Describe the morphology of the red blood cells.
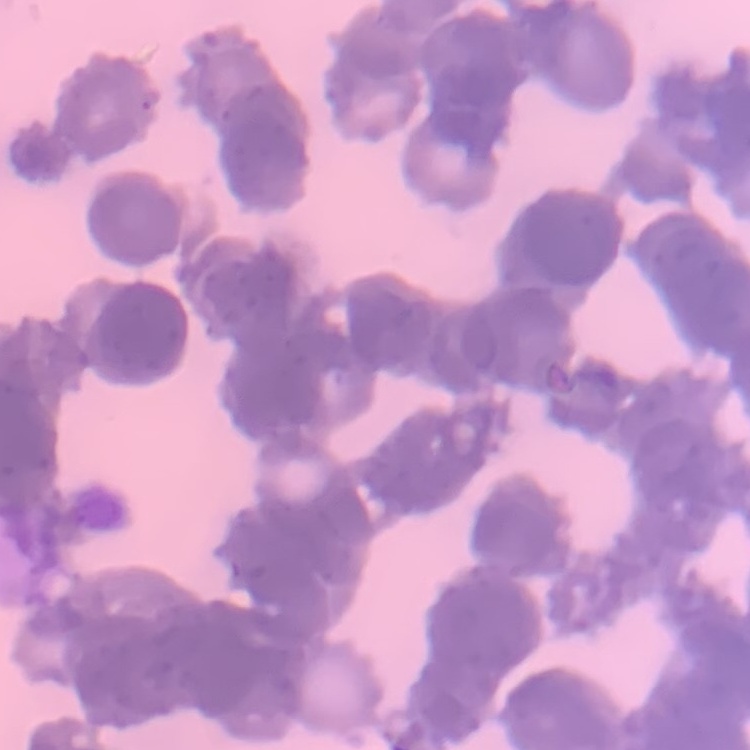

They show rouleaux formation.

Summary:
  - Image type: square crop of a larger photomicrograph
  - Stain: Field's or Giemsa
  - Preparation: thin blood smear